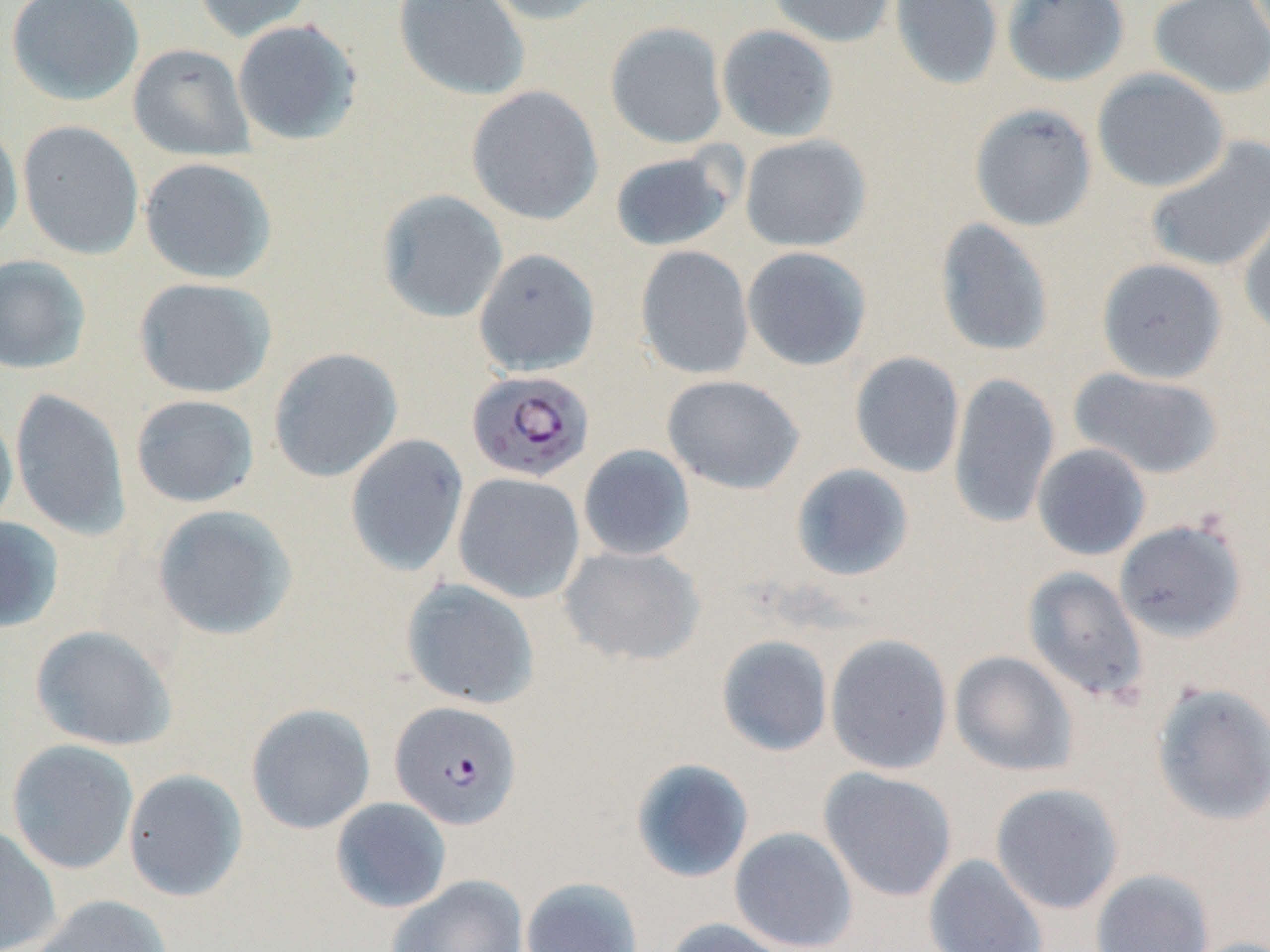
Approximate bounding boxes as [x1, y1, x2, y2] in pixels. Uninfected red blood cell locations: [6, 0, 144, 107], [192, 0, 314, 43], [393, 0, 531, 102], [483, 0, 613, 25], [767, 0, 896, 47], [889, 0, 1003, 90], [1002, 0, 1129, 86], [1149, 0, 1270, 99], [232, 19, 362, 146], [605, 21, 728, 149], [716, 24, 839, 142], [127, 43, 255, 161], [1092, 68, 1231, 193], [466, 86, 603, 225], [969, 103, 1098, 232], [17, 120, 144, 259], [0, 123, 24, 248], [739, 134, 871, 252], [1144, 136, 1270, 275], [609, 149, 738, 252], [139, 157, 277, 284], [376, 189, 508, 324], [1238, 199, 1270, 339], [934, 217, 1055, 357], [635, 245, 755, 380], [742, 246, 872, 371], [473, 248, 600, 376], [0, 254, 91, 375], [1096, 257, 1228, 384], [133, 276, 277, 398], [268, 347, 403, 482], [850, 352, 965, 478], [1068, 367, 1224, 480], [947, 373, 1060, 529], [661, 374, 804, 495], [9, 388, 131, 542], [130, 394, 259, 508], [0, 400, 18, 535], [345, 433, 469, 576], [1032, 443, 1151, 561], [578, 444, 695, 561], [790, 463, 914, 581], [453, 472, 585, 604], [151, 504, 298, 641], [0, 517, 64, 633], [1114, 518, 1248, 642], [558, 544, 705, 666], [1022, 566, 1148, 703], [400, 578, 540, 710], [29, 624, 176, 751], [825, 633, 953, 775], [716, 635, 834, 756], [949, 651, 1079, 777], [1150, 681, 1270, 826], [246, 703, 376, 834], [6, 739, 139, 875], [630, 758, 754, 883], [818, 767, 958, 902], [122, 768, 248, 901], [990, 783, 1124, 914], [330, 797, 452, 913], [0, 825, 61, 951], [729, 826, 858, 951], [923, 854, 1049, 952], [1091, 868, 1215, 952], [387, 874, 529, 952], [519, 877, 644, 952], [30, 894, 173, 952], [662, 918, 796, 952]. Plasmodium falciparum-infected red blood cell locations: [466, 370, 595, 483], [389, 700, 522, 830]. Slide-level diagnosis: Plasmodium falciparum. One field of a larger specimen. Light microscopy. Image is 1270×952 pixels. May-Grünwald-Giemsa stain. 1000x magnification. Thin blood smear.